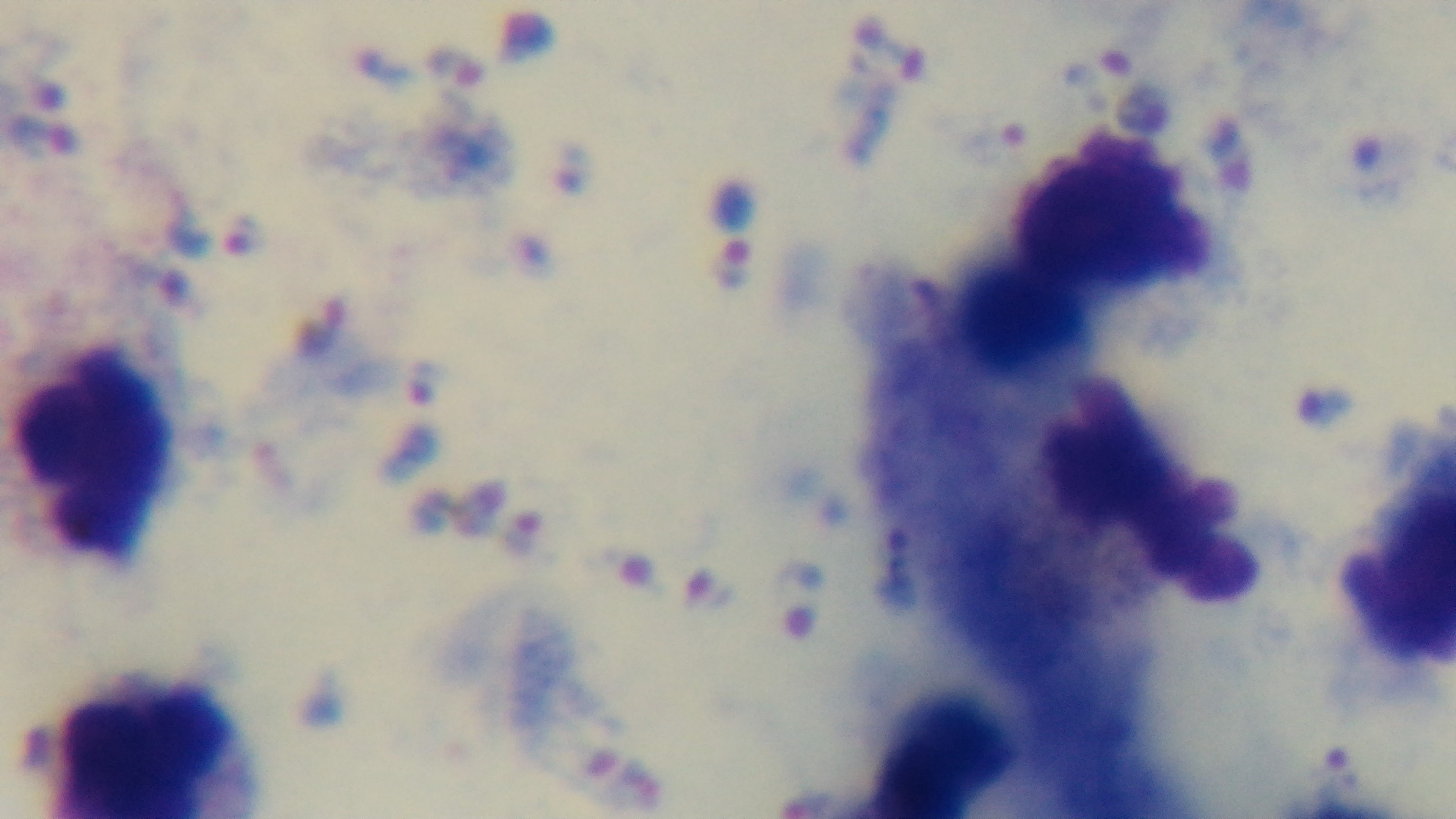 Mounted 4K digital camera. Light microscopy. Giemsa-stained. Preparation: thick. Single field of view. 100x oil-immersion objective. Malaria status: infected.